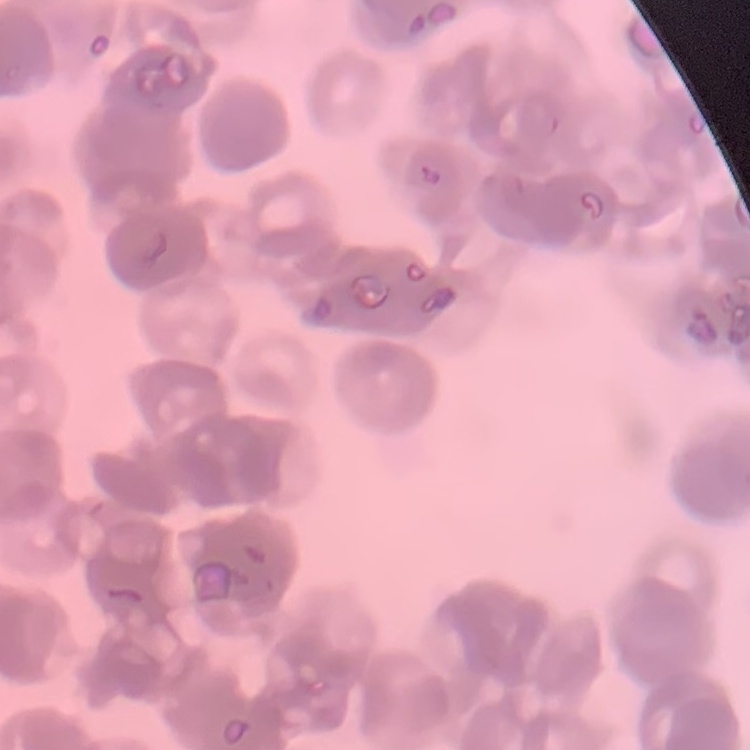
Summary:
  - Erythrocyte morphology: rouleaux formation
  - Preparation: thin blood film
  - Image type: square crop of a larger photomicrograph
  - Stain: Field's or Giemsa